Identify the parasite.
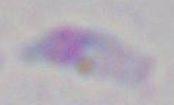
This is Toxoplasma gondii.

Micrograph. Captured at 1000x magnification.